Classify this cell by malaria status.
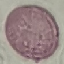

It is uninfected.

Thin blood film. Cell patch, automatically extracted from a larger field of view and resized to 64 × 64 pixels. Giemsa-stained preparation. Acquired by smartphone through the microscope eyepiece.